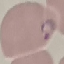 Malaria status: parasitized. Thin blood smear. Automatically extracted cell patch, resized to 64 × 64 pixels. Giemsa-stained preparation. Acquired by smartphone through the microscope eyepiece.